Identify the preparation type.
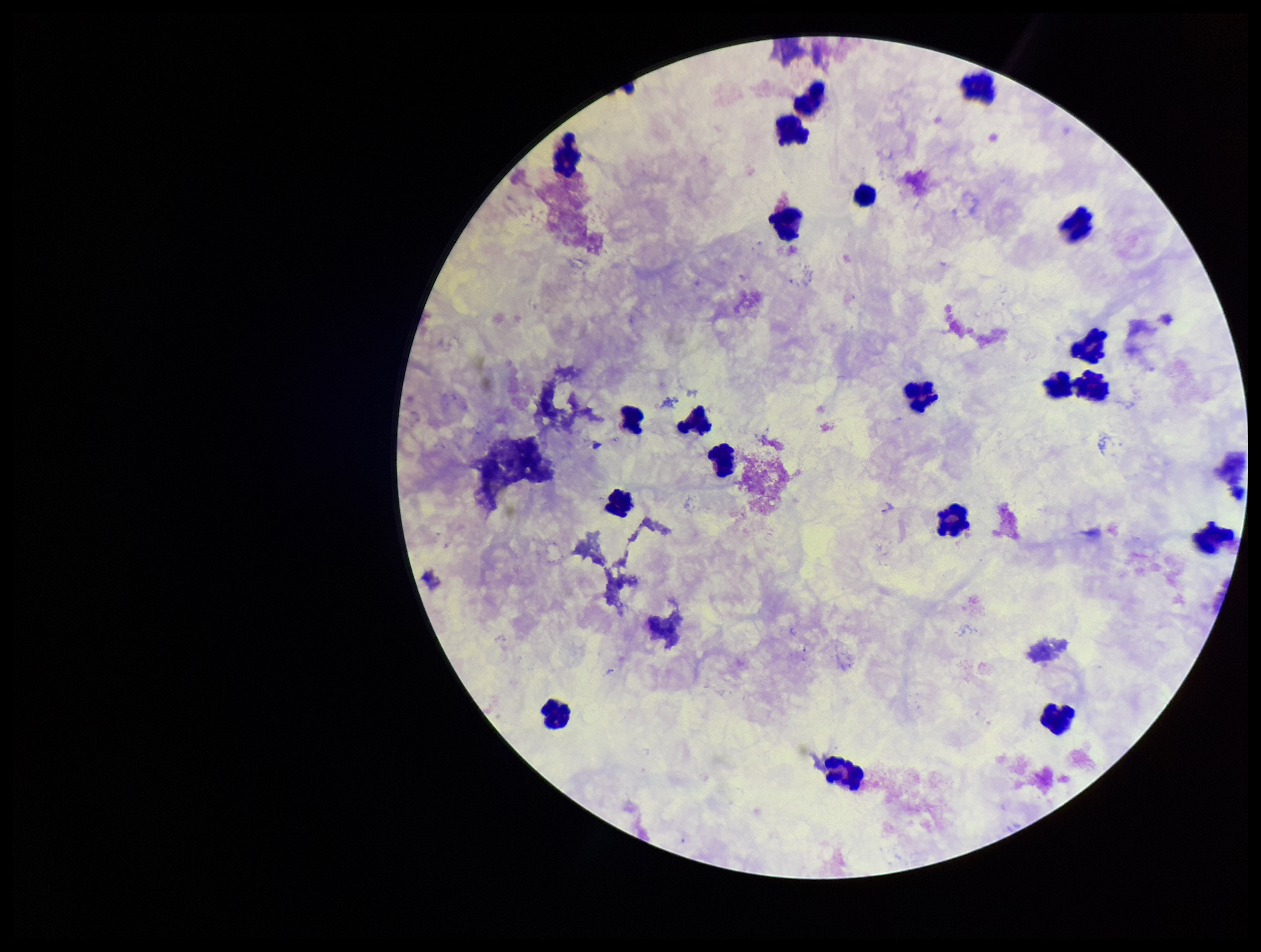

A thick smear.

Leukocyte count: 18. Smartphone photograph taken through the eyepiece of a microscope. One field from this slide. Plasmodium parasites: none identified. Stained with Giemsa. Patient malaria status: negative. Image is 1261×952 pixels. Parasite count: 0.